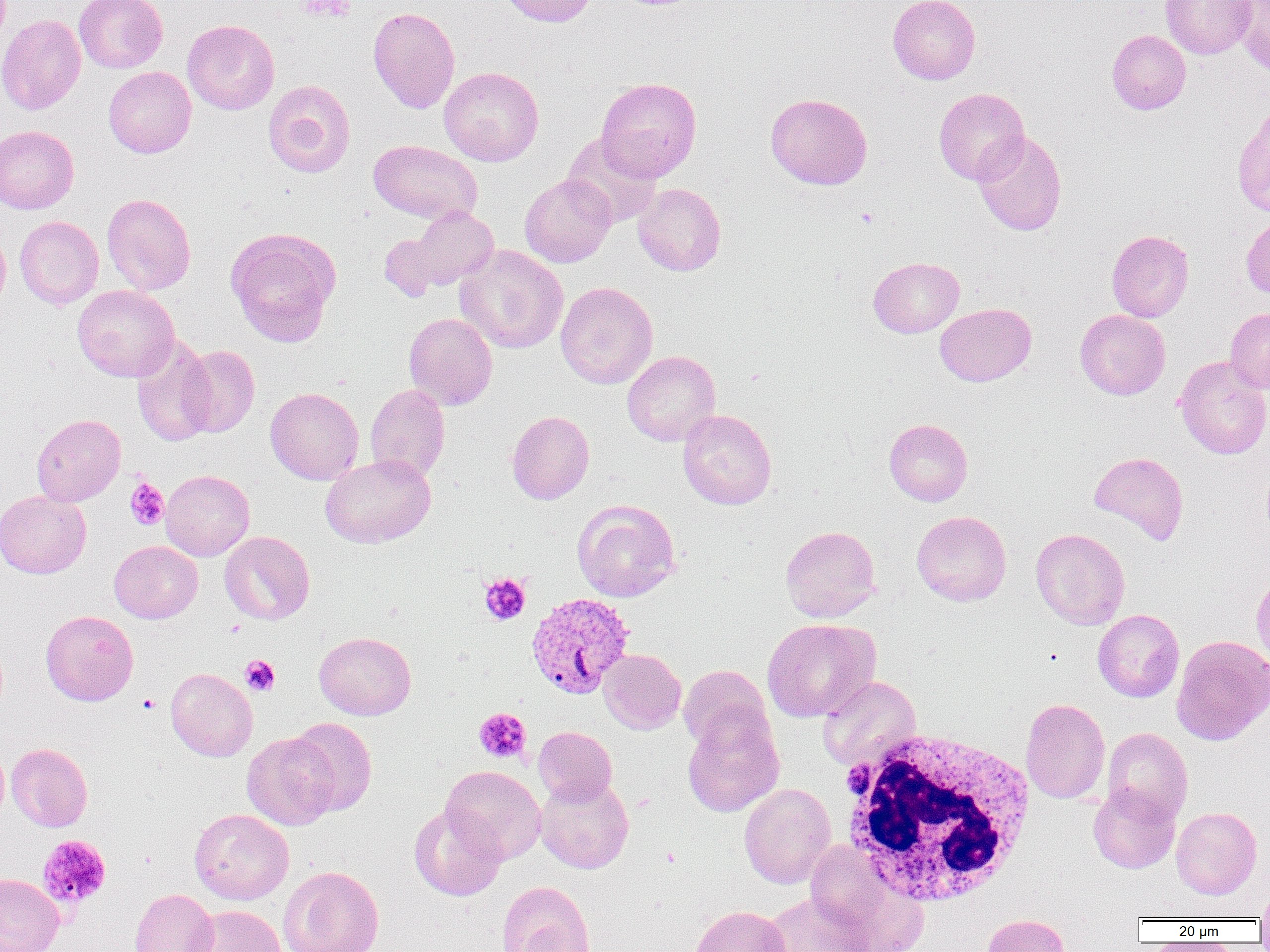

Summary:
  - Coordinate format: approximate bounding boxes as named x1/y1/x2/y2 corners in pixels
  - White blood cell locations: (x1=837, y1=728, x2=1037, y2=909)
  - Platelet locations: (x1=301, y1=0, x2=354, y2=21), (x1=125, y1=478, x2=169, y2=530), (x1=479, y1=572, x2=531, y2=625), (x1=240, y1=655, x2=280, y2=696), (x1=138, y1=694, x2=160, y2=714), (x1=474, y1=708, x2=531, y2=763), (x1=37, y1=834, x2=112, y2=910)
  - Plasmodium vivax-infected red blood cell locations: (x1=525, y1=592, x2=636, y2=699)
  - Uninfected red blood cell locations: (x1=74, y1=0, x2=168, y2=73), (x1=499, y1=0, x2=598, y2=27), (x1=887, y1=0, x2=980, y2=85), (x1=1160, y1=0, x2=1256, y2=59), (x1=1234, y1=0, x2=1270, y2=77), (x1=368, y1=6, x2=460, y2=114), (x1=0, y1=14, x2=86, y2=115), (x1=182, y1=19, x2=280, y2=114), (x1=1106, y1=30, x2=1191, y2=115), (x1=103, y1=66, x2=196, y2=158), (x1=438, y1=66, x2=544, y2=166), (x1=596, y1=77, x2=701, y2=182), (x1=263, y1=80, x2=356, y2=178), (x1=933, y1=88, x2=1029, y2=184), (x1=765, y1=93, x2=872, y2=190), (x1=1232, y1=104, x2=1270, y2=219), (x1=0, y1=125, x2=79, y2=214), (x1=971, y1=130, x2=1067, y2=235), (x1=561, y1=133, x2=662, y2=227), (x1=368, y1=140, x2=482, y2=224), (x1=520, y1=174, x2=616, y2=267), (x1=633, y1=183, x2=726, y2=276), (x1=101, y1=193, x2=196, y2=294), (x1=398, y1=207, x2=500, y2=293), (x1=1241, y1=214, x2=1270, y2=300), (x1=14, y1=216, x2=104, y2=309), (x1=0, y1=225, x2=11, y2=317), (x1=225, y1=227, x2=341, y2=346), (x1=379, y1=230, x2=452, y2=302), (x1=1106, y1=230, x2=1194, y2=322), (x1=455, y1=245, x2=568, y2=354), (x1=868, y1=257, x2=964, y2=337), (x1=555, y1=281, x2=658, y2=389), (x1=73, y1=285, x2=179, y2=382), (x1=935, y1=303, x2=1036, y2=386), (x1=1225, y1=307, x2=1270, y2=394), (x1=1075, y1=309, x2=1170, y2=400), (x1=404, y1=312, x2=497, y2=410), (x1=131, y1=335, x2=217, y2=447), (x1=178, y1=345, x2=260, y2=437), (x1=622, y1=350, x2=720, y2=446), (x1=1174, y1=356, x2=1270, y2=459), (x1=365, y1=383, x2=450, y2=483), (x1=265, y1=387, x2=364, y2=485), (x1=678, y1=409, x2=776, y2=510), (x1=507, y1=410, x2=594, y2=504), (x1=31, y1=414, x2=126, y2=506), (x1=884, y1=419, x2=973, y2=506), (x1=1089, y1=451, x2=1189, y2=545), (x1=320, y1=454, x2=436, y2=548), (x1=161, y1=469, x2=254, y2=561), (x1=0, y1=490, x2=91, y2=579), (x1=572, y1=499, x2=681, y2=602), (x1=911, y1=511, x2=1011, y2=606), (x1=780, y1=525, x2=881, y2=622), (x1=1031, y1=528, x2=1130, y2=629), (x1=219, y1=531, x2=315, y2=624), (x1=109, y1=541, x2=202, y2=623), (x1=1251, y1=571, x2=1270, y2=669), (x1=1093, y1=609, x2=1184, y2=702), (x1=40, y1=610, x2=139, y2=706), (x1=762, y1=618, x2=880, y2=722), (x1=314, y1=631, x2=416, y2=720), (x1=1171, y1=634, x2=1270, y2=746), (x1=598, y1=649, x2=686, y2=734), (x1=678, y1=665, x2=772, y2=753), (x1=166, y1=667, x2=258, y2=761), (x1=817, y1=676, x2=921, y2=771), (x1=1020, y1=698, x2=1110, y2=804), (x1=682, y1=706, x2=784, y2=817), (x1=287, y1=718, x2=377, y2=816), (x1=533, y1=726, x2=617, y2=805), (x1=1102, y1=727, x2=1192, y2=823), (x1=241, y1=732, x2=338, y2=830), (x1=0, y1=741, x2=8, y2=829), (x1=6, y1=743, x2=92, y2=832), (x1=441, y1=765, x2=546, y2=864), (x1=535, y1=775, x2=634, y2=874), (x1=739, y1=783, x2=836, y2=888), (x1=1088, y1=784, x2=1181, y2=874), (x1=409, y1=805, x2=506, y2=901), (x1=1171, y1=807, x2=1262, y2=899), (x1=189, y1=809, x2=294, y2=904), (x1=806, y1=843, x2=929, y2=952), (x1=278, y1=865, x2=384, y2=952), (x1=0, y1=873, x2=64, y2=952), (x1=496, y1=881, x2=593, y2=951), (x1=1256, y1=885, x2=1270, y2=926), (x1=130, y1=889, x2=218, y2=952), (x1=761, y1=892, x2=871, y2=952), (x1=188, y1=905, x2=287, y2=952), (x1=689, y1=905, x2=792, y2=952), (x1=980, y1=914, x2=1072, y2=952)
  - Slide-level diagnosis: Plasmodium vivax
  - Field of view: single
  - Magnification: 1000x
  - Preparation: thin blood film
  - Image size: 1270×952 pixels
  - Modality: optical microscopy